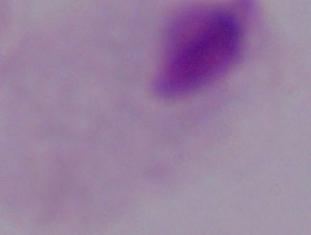

A trichomonad is seen. Captured at 1000x magnification. Micrograph.